Report the malaria status of this cell.
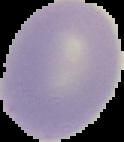
Uninfected.

image size = 124×142 pixels
preparation = thin blood film
image type = segmented cell region with the area outside set to black